Classify this cell by malaria status.
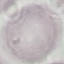

It is uninfected.

capture = smartphone camera at the microscope eyepiece
stain = Giemsa
preparation = thin smear
image type = automatically extracted cell patch, resized to 64 × 64 pixels